Describe the morphology of the erythrocytes.
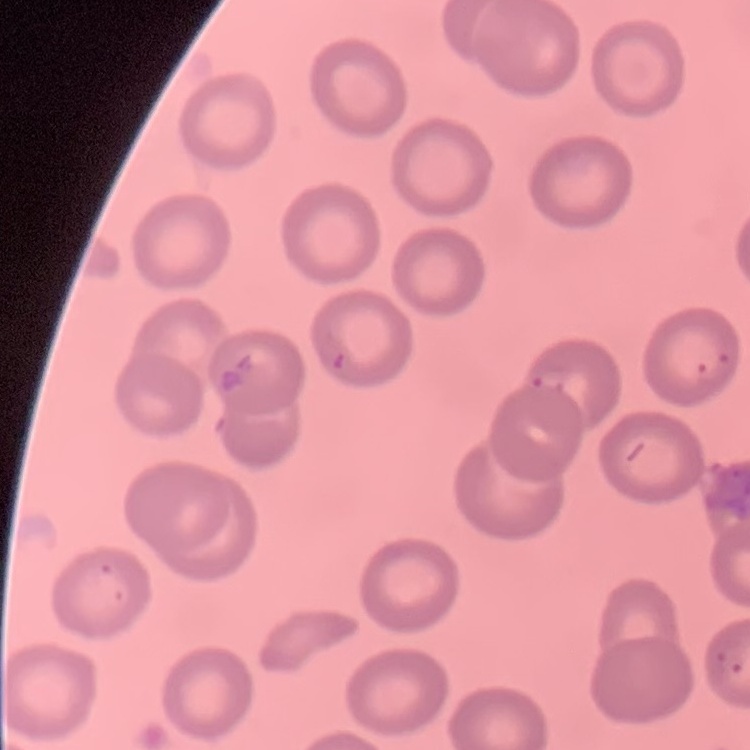

No rouleaux formation.

stain: Field's or Giemsa
image_type: square crop of a larger photomicrograph
preparation: thin blood smear